Locate every Plasmodium falciparum-infected red blood cell.
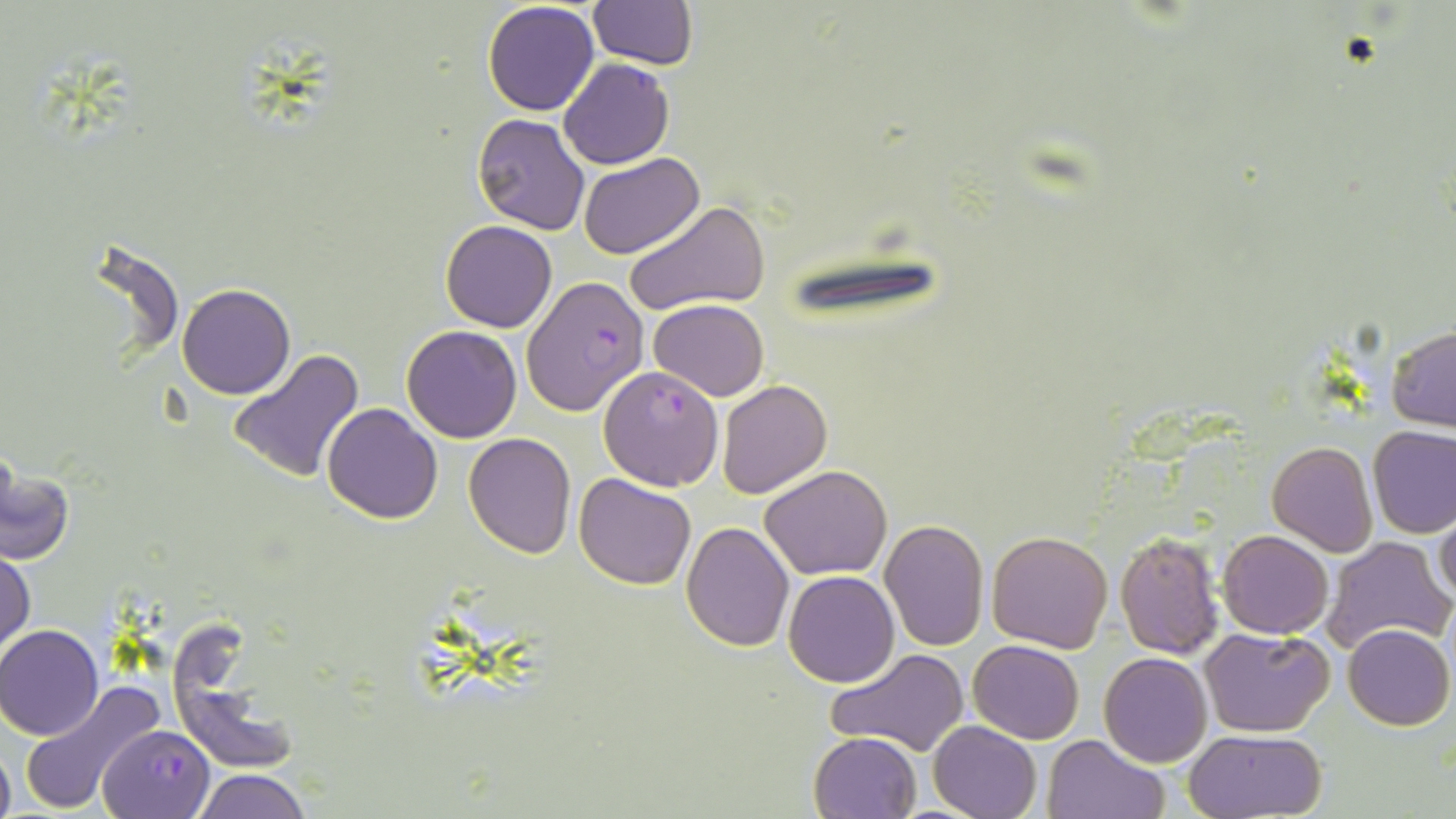

Approximate bounding boxes as [x1, y1, x2, y2] in pixels.
Plasmodium falciparum-infected red blood cells: [522, 274, 648, 417], [98, 726, 214, 818].

Summary:
  - Uninfected red blood cell locations: [587, 0, 699, 69], [482, 2, 600, 116], [557, 59, 673, 169], [472, 113, 591, 236], [578, 152, 704, 258], [624, 201, 771, 316], [440, 221, 558, 333], [176, 282, 297, 399], [647, 299, 769, 401], [402, 326, 523, 443], [1386, 327, 1456, 430], [228, 349, 365, 485], [597, 366, 726, 492], [716, 379, 832, 498], [321, 403, 443, 525], [1367, 425, 1456, 538], [462, 433, 576, 558], [1266, 441, 1377, 555], [1, 464, 74, 567], [761, 465, 891, 580], [573, 473, 697, 589], [704, 486, 875, 613], [1434, 509, 1456, 609], [879, 519, 989, 651], [680, 521, 795, 651], [986, 530, 1113, 653], [1114, 530, 1226, 660], [1218, 531, 1333, 639], [1322, 536, 1454, 653], [1, 550, 35, 655], [784, 571, 900, 688], [1342, 624, 1453, 731], [0, 625, 104, 740], [1200, 626, 1335, 736], [968, 640, 1085, 743], [826, 648, 970, 757], [1099, 652, 1213, 767], [18, 679, 165, 814], [929, 721, 1041, 819], [1183, 728, 1327, 818], [808, 732, 922, 819], [1044, 734, 1165, 819], [0, 742, 14, 819], [193, 768, 311, 819]
  - Slide-level diagnosis: Plasmodium falciparum
  - Preparation: thin blood film
  - Magnification: 1000x
  - Image size: 1456×819 pixels
  - Stain: May-Grünwald-Giemsa
  - Field of view: one of a larger specimen
  - Modality: optical microscopy